Give the position of every malaria parasite.
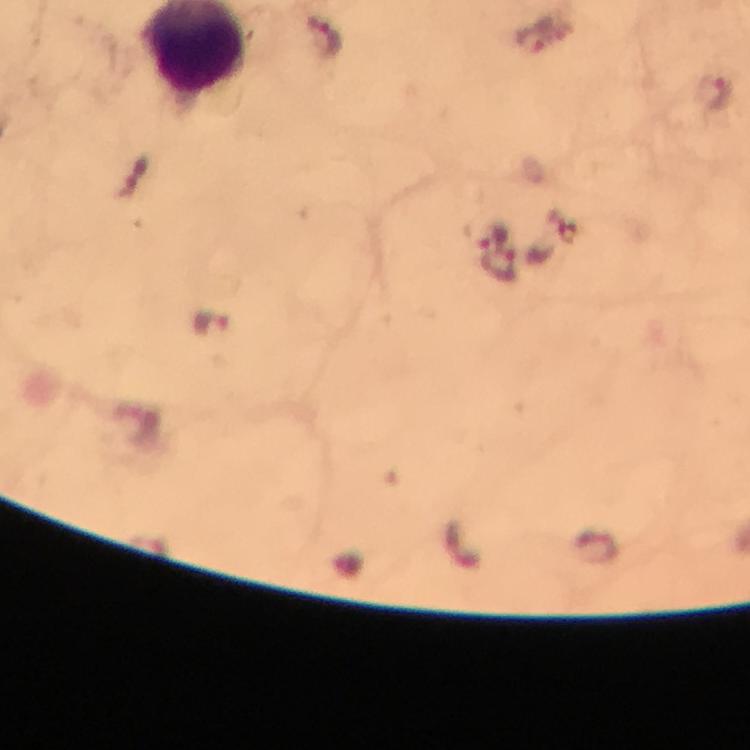
Approximate centers as (x, y) in pixels.
Malaria parasites: (324, 33), (533, 43), (714, 97), (495, 235), (499, 264), (212, 323).

stain: Giemsa
image_size: 750×750 pixels
context: from a malaria diagnostic workup
immersion_oil: applied
capture: smartphone mounted on the microscope
cropped_from: one field of view
magnification: 100x
preparation: thick blood film